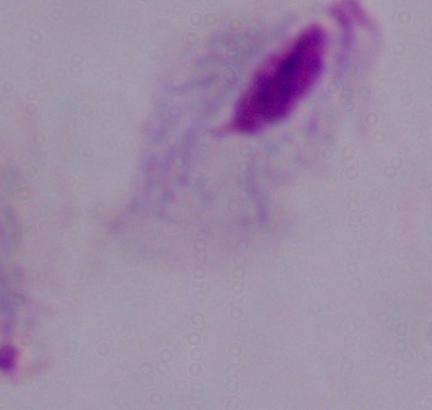 1000x magnification. Micrograph. A trichomonad is shown.